Classify this cell by malaria status.
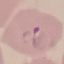

Parasitized.

stain = Giemsa
image type = automatically extracted cell patch, resized to 64 × 64 pixels
preparation = thin blood smear
capture = smartphone camera at the microscope eyepiece